Point out each leukocyte.
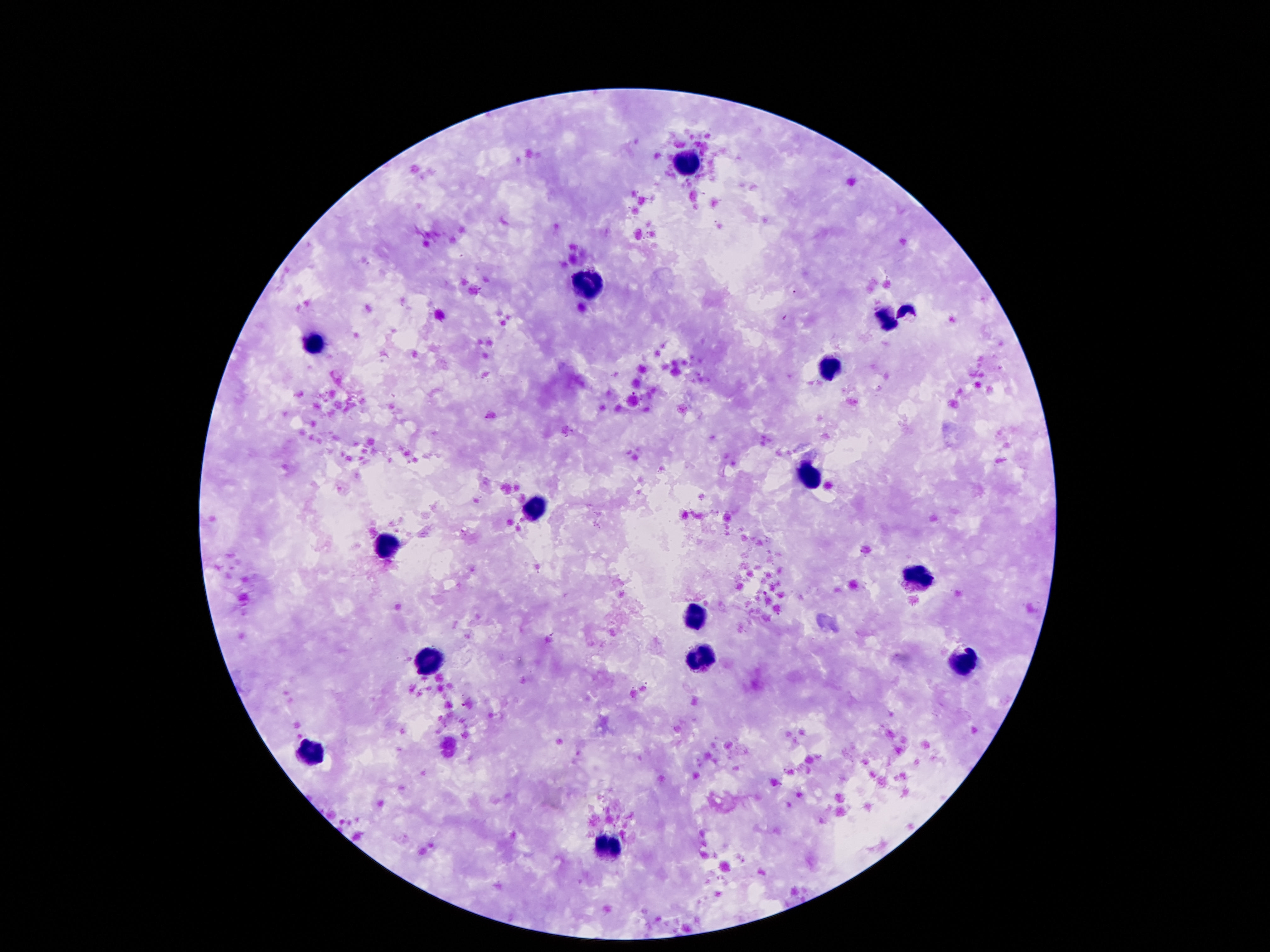

Approximate centers as (x, y) in pixels.
Leukocytes: (687, 163), (586, 283), (884, 320), (313, 341), (832, 365), (808, 478), (538, 507), (386, 541), (918, 576), (693, 616), (701, 658), (962, 663), (428, 665), (309, 753), (607, 847).

Image is 1270×952 pixels. Giemsa stain. Photographed through the microscope eyepiece with a smartphone camera. Single field of view. 100x magnification. Thick peripheral-blood smear. Patient malaria status: uninfected.